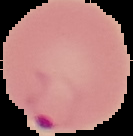
Summary:
  - Result: malaria parasites identified
  - Image size: 133×136 pixels
  - Image type: segmented cell region on a black background
  - Preparation: thin blood film